Identify the parasite.
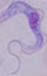
A trypanosome.

modality: photomicrograph
magnification: 1000x